Assess this cell for malaria.
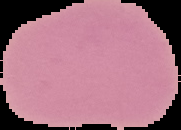

It is uninfected.

Summary:
  - Preparation: thin blood smear
  - Image type: segmented cell region on a black background
  - Image size: 181×130 pixels